Report the malaria status.
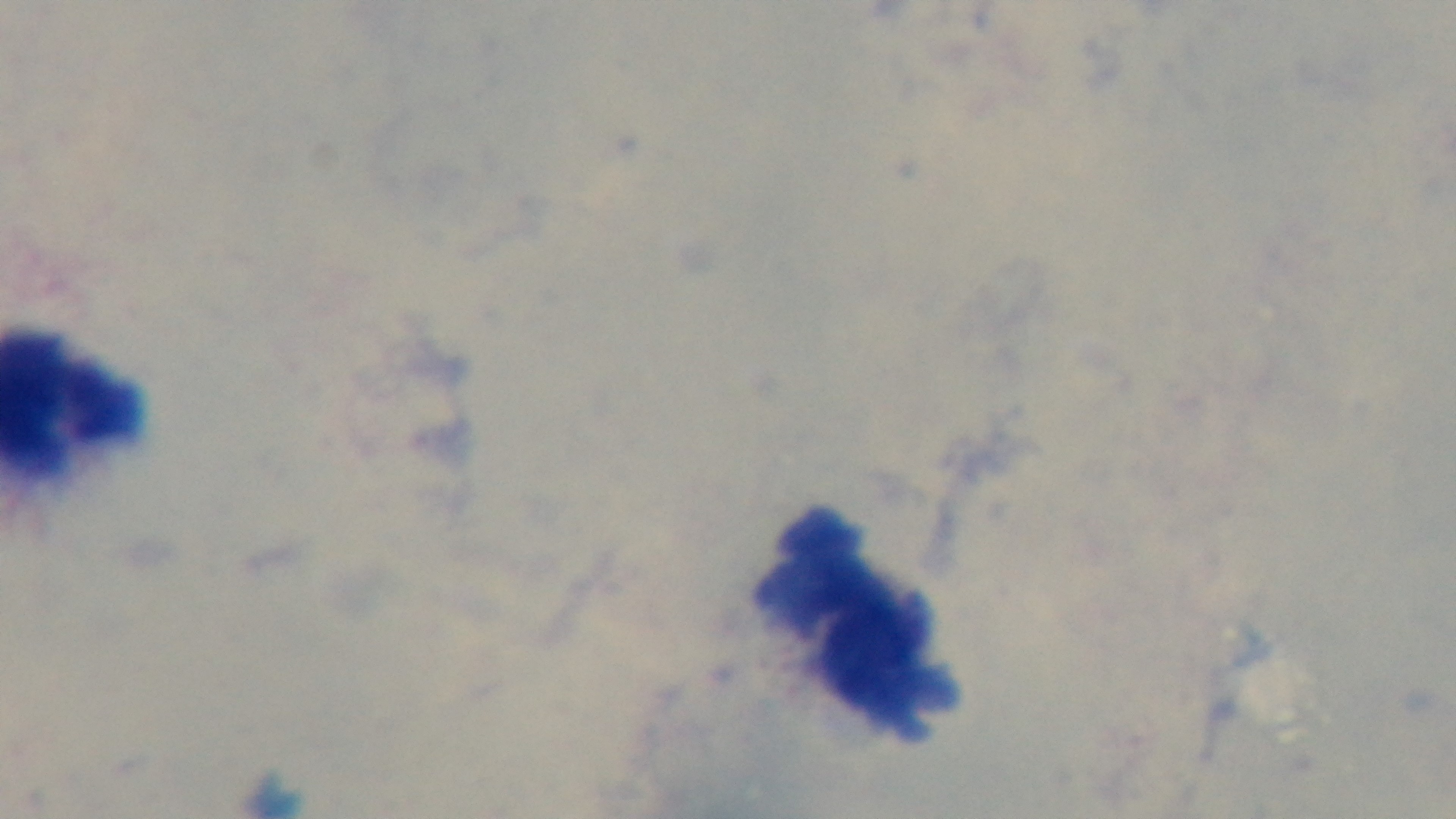

Negative.

One field from the slide. Oil-immersion objective, 100x. Giemsa-stained. Light microscopy. Preparation: thick blood film. Mounted 4K digital camera.